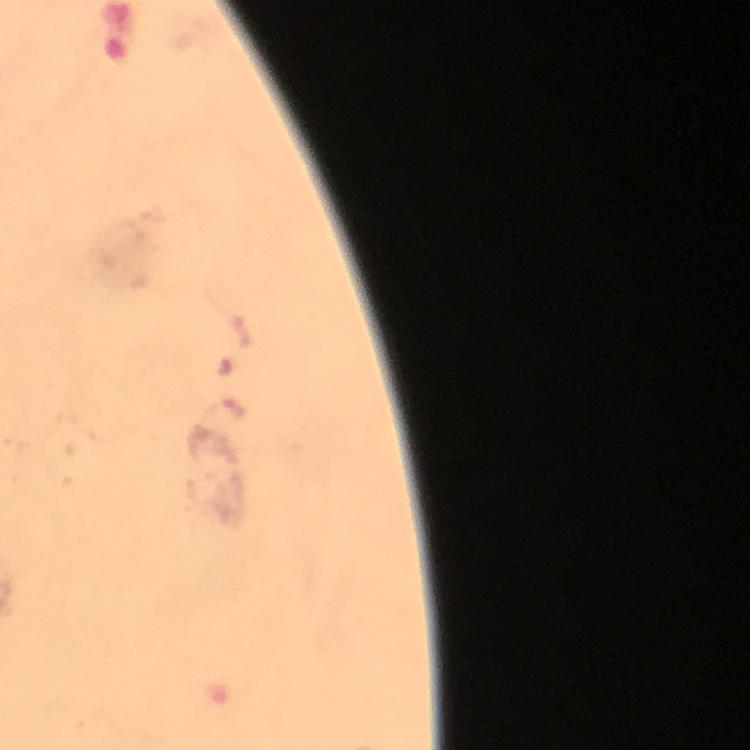
Approximate object centers, in pixels from the top-left corner.
Summary:
  - Malaria parasite locations: (x=226, y=367), (x=224, y=416)
  - Capture: smartphone photograph through a microscope
  - Preparation: thick blood smear
  - Cropped from: a single field of view
  - Magnification: 100x
  - Stain: Giemsa
  - Image size: 750×750 pixels
  - Immersion oil: applied
  - Context: from a diagnostic examination for malaria